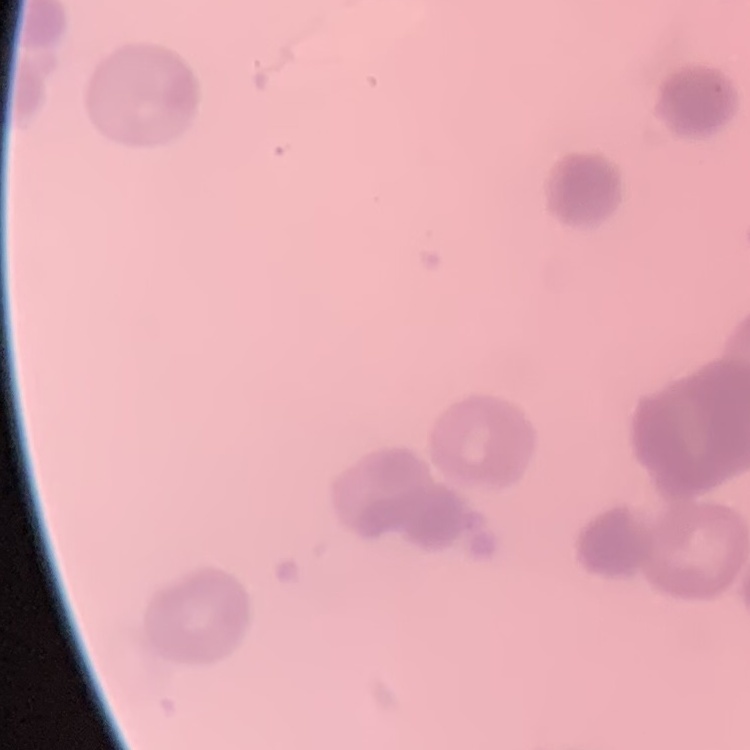
red blood cell morphology = rouleaux formation
stain = Field's or Giemsa
preparation = thin peripheral smear
image type = square crop of a larger photomicrograph